Assess this cell for malaria.
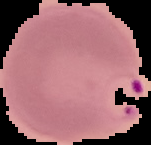
It is parasitized.

Summary:
  - Image type: cell region segmented out of the field of view; surrounding area masked to black
  - Preparation: thin blood film
  - Image size: 151×145 pixels